Report the malaria status of this cell.
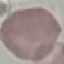

Uninfected.

Summary:
  - Preparation: thin smear
  - Capture: smartphone camera at the microscope eyepiece
  - Stain: Giemsa
  - Image type: cell patch, automatically extracted from a larger field of view and resized to 64 × 64 pixels